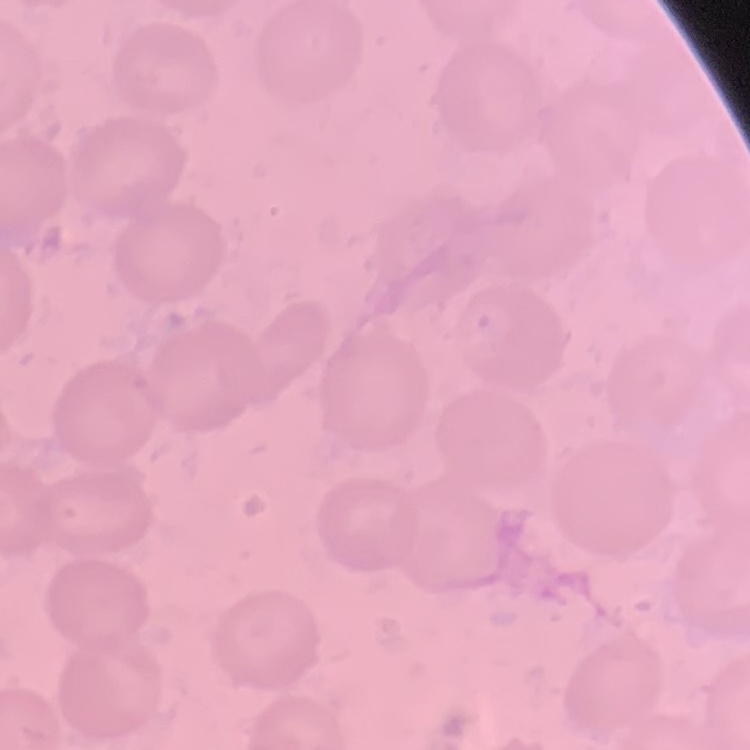
erythrocyte_morphology: no rouleaux formation
preparation: thin peripheral smear
image_type: one tile cut from a larger photomicrograph
stain: Field's or Giemsa